Assess this cell for malaria.
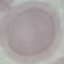

Uninfected.

Summary:
  - Preparation: thin smear
  - Image type: cell patch, automatically extracted from a larger field of view and resized to 64 × 64 pixels
  - Capture: smartphone camera at the microscope eyepiece
  - Stain: Giemsa